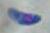
{
  "modality": "micrograph",
  "identification": "Toxoplasma gondii",
  "magnification": "1000x"
}